Identify the parasite.
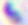

This is Toxoplasma gondii.

magnification = 400x
modality = micrograph